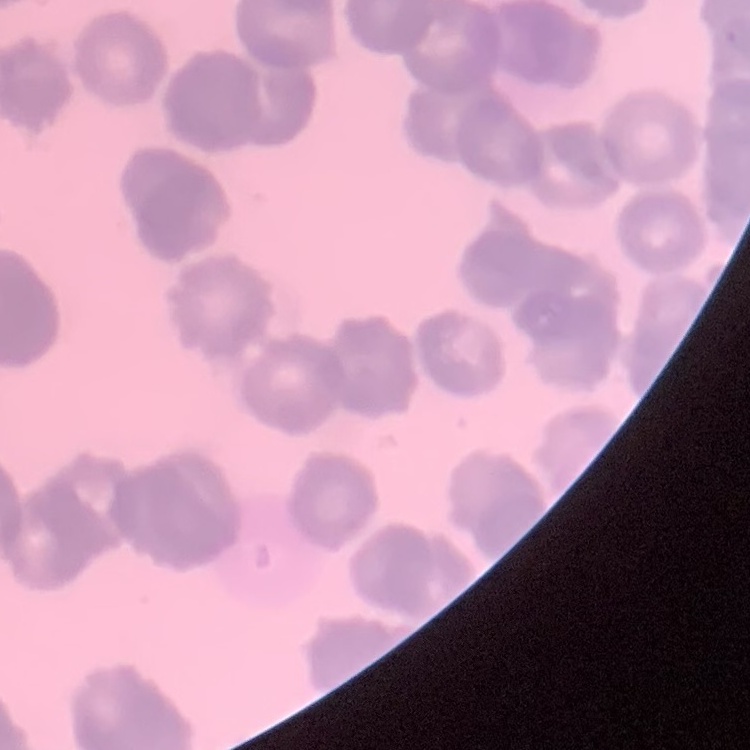

The red blood cells show rouleaux formation. One tile cut from a larger photomicrograph. Stained with either Field's or Giemsa. Thin blood film.